Point out each malaria parasite and classify it by life-cycle stage.
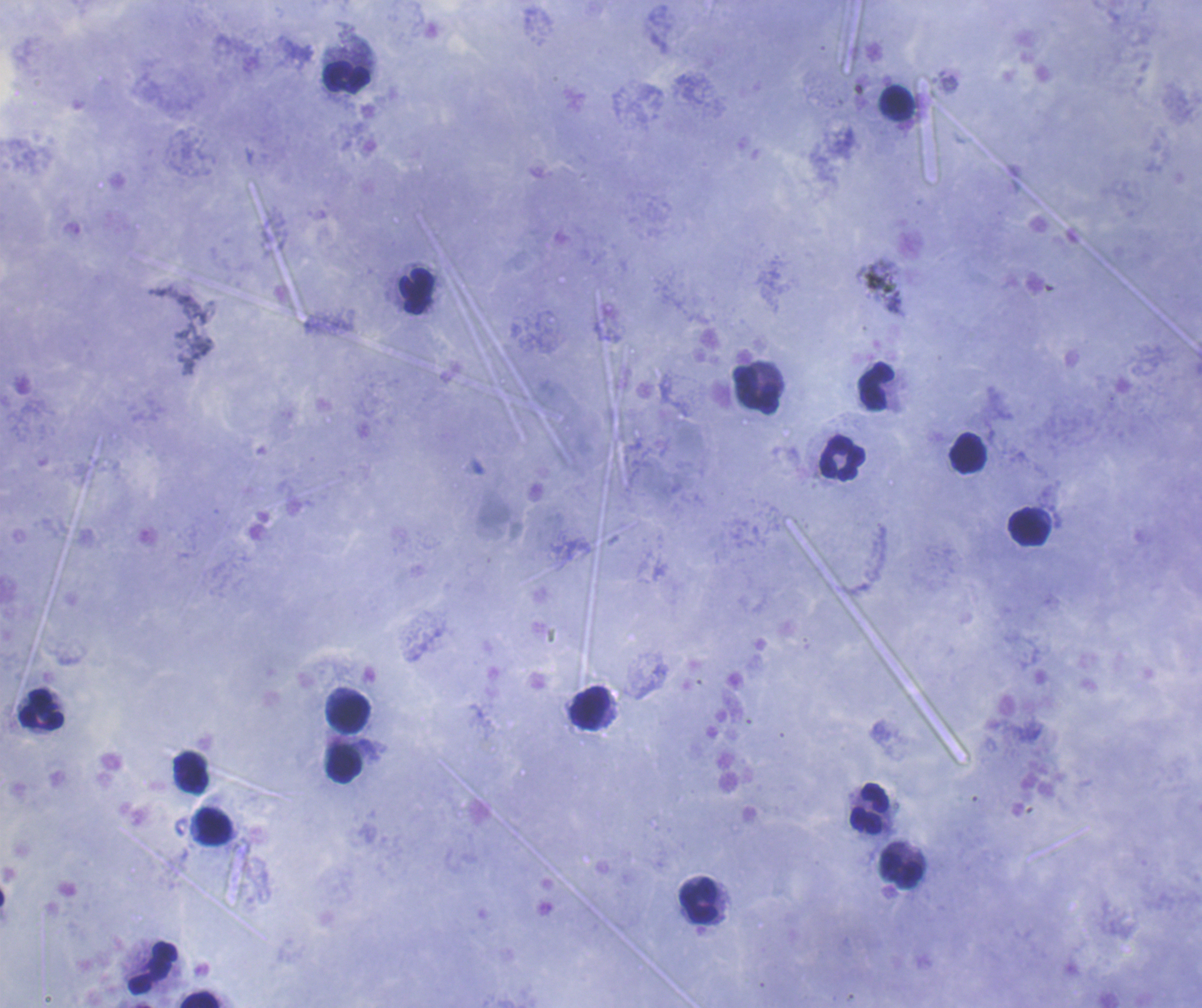

Negative for malaria parasites.

Approximate centers as (x, y) in pixels.
Summary:
  - Leukocyte locations: (347, 77), (895, 101), (417, 291), (876, 385), (756, 390), (968, 452), (843, 458), (1029, 527), (590, 708), (41, 709), (348, 714), (344, 765), (192, 772), (870, 809), (214, 826), (901, 871), (698, 901), (153, 967), (199, 999)
  - Background quality: good
  - Coloration quality: good
  - Field of view: single
  - Context: previously used in an actual diagnosis
  - Magnification: 100x
  - Preparation: thick blood film
  - Stain: Romanowsky
  - Image size: 1202×1008 pixels